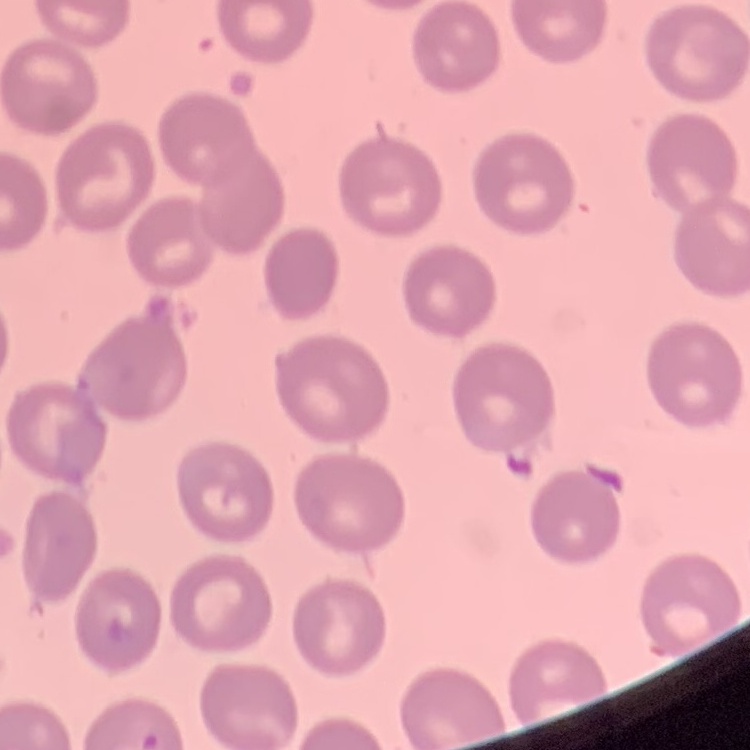 The red blood cells exhibit no rouleaux formation. Field's or Giemsa stain. One tile cut from a larger photomicrograph. Thin peripheral smear.